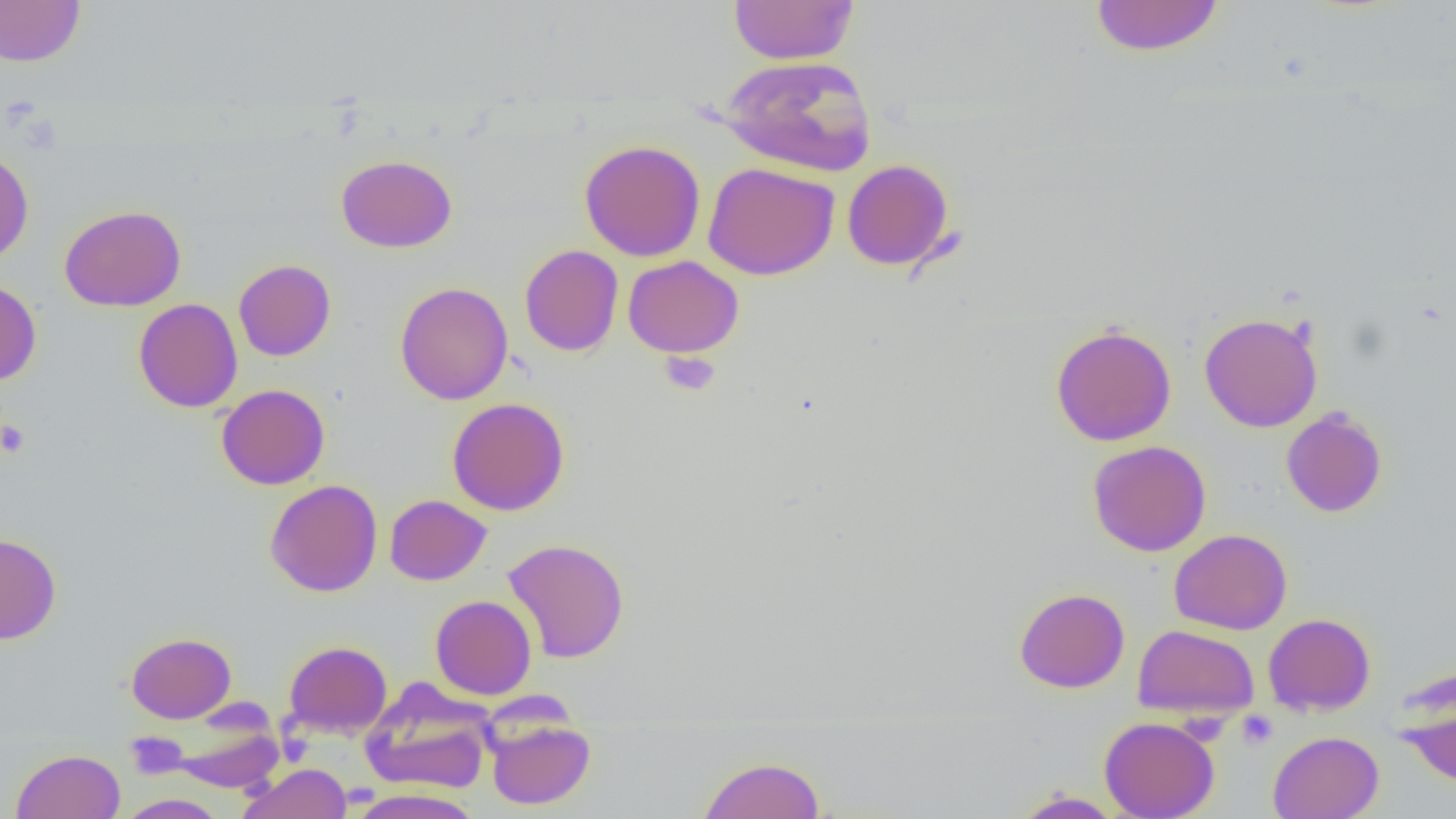
Summary:
  - Coordinate format: approximate bounding boxes as named x1/y1/x2/y2 corners in pixels
  - Uninfected red blood cell locations: (x1=729, y1=0, x2=859, y2=65), (x1=1090, y1=0, x2=1224, y2=57), (x1=0, y1=1, x2=85, y2=67), (x1=717, y1=55, x2=876, y2=176), (x1=578, y1=139, x2=706, y2=262), (x1=0, y1=148, x2=34, y2=267), (x1=336, y1=155, x2=457, y2=252), (x1=842, y1=159, x2=955, y2=271), (x1=702, y1=161, x2=840, y2=280), (x1=59, y1=204, x2=186, y2=312), (x1=520, y1=245, x2=623, y2=357), (x1=623, y1=255, x2=744, y2=358), (x1=233, y1=259, x2=336, y2=361), (x1=0, y1=279, x2=41, y2=385), (x1=394, y1=281, x2=513, y2=405), (x1=133, y1=298, x2=243, y2=412), (x1=1198, y1=312, x2=1324, y2=432), (x1=1050, y1=323, x2=1177, y2=447), (x1=216, y1=384, x2=330, y2=490), (x1=447, y1=397, x2=569, y2=515), (x1=1281, y1=407, x2=1387, y2=518), (x1=1087, y1=441, x2=1211, y2=557), (x1=265, y1=479, x2=383, y2=597), (x1=384, y1=494, x2=491, y2=585), (x1=1169, y1=528, x2=1292, y2=635), (x1=0, y1=533, x2=61, y2=645), (x1=502, y1=537, x2=630, y2=664), (x1=1014, y1=587, x2=1129, y2=693), (x1=430, y1=595, x2=537, y2=700), (x1=1263, y1=613, x2=1376, y2=716), (x1=1133, y1=624, x2=1260, y2=720), (x1=126, y1=632, x2=235, y2=723), (x1=283, y1=640, x2=392, y2=738), (x1=1395, y1=676, x2=1456, y2=791), (x1=361, y1=683, x2=493, y2=794), (x1=1099, y1=716, x2=1220, y2=819), (x1=170, y1=717, x2=285, y2=793), (x1=486, y1=718, x2=595, y2=810), (x1=124, y1=731, x2=189, y2=779), (x1=1268, y1=731, x2=1384, y2=819), (x1=11, y1=749, x2=125, y2=819), (x1=698, y1=755, x2=826, y2=819), (x1=238, y1=763, x2=352, y2=819), (x1=348, y1=788, x2=483, y2=819), (x1=1011, y1=790, x2=1125, y2=818), (x1=115, y1=794, x2=229, y2=818)
  - Platelet locations: (x1=0, y1=419, x2=30, y2=458), (x1=1237, y1=710, x2=1278, y2=749), (x1=124, y1=732, x2=188, y2=780)
  - Slide-level diagnosis: no evidence of blood parasites
  - Magnification: 1000x
  - Preparation: thin blood smear
  - Image size: 1456×819 pixels
  - Field of view: one of a larger specimen
  - Modality: light microscopy